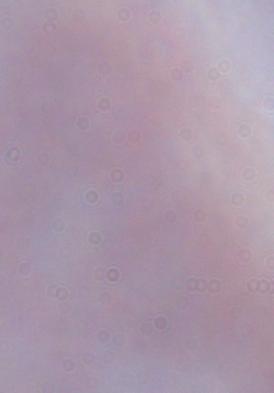
modality = photomicrograph
identification = trypanosome
magnification = 1000x